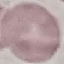

Result: negative for malaria parasites. Thin blood smear. Cell patch, automatically extracted from a larger field of view and resized to 64 × 64 pixels. Acquired by smartphone through the microscope eyepiece. Giemsa-stained preparation.